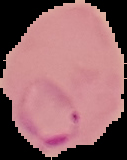

malaria_status: parasitized
image_type: cell region segmented out of the field of view; surrounding area masked to black
image_size: 127×160 pixels
preparation: thin blood film